Assess this cell for malaria.
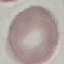
It is uninfected.

Giemsa stain. Photographed with a smartphone camera at the microscope eyepiece. Automatically extracted cell patch, resized to 64 × 64 pixels. Thin blood smear.